Locate every Plasmodium parasite.
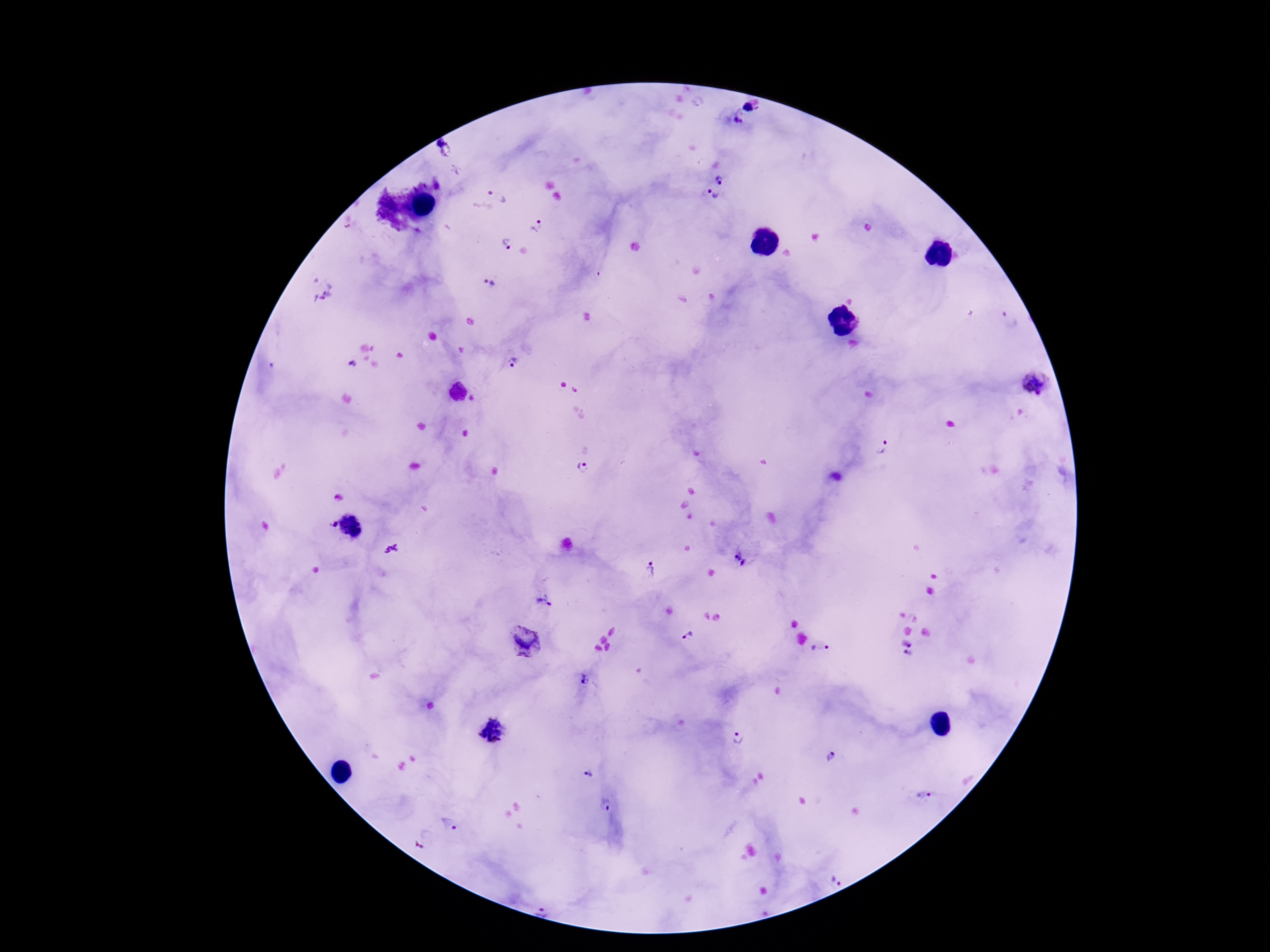
Approximate centers as {x, y} in pixels.
Plasmodium parasites: {748, 107}, {739, 123}, {444, 146}, {721, 181}, {499, 190}, {712, 196}, {537, 225}, {505, 244}, {490, 284}, {1009, 319}, {513, 363}, {352, 365}, {1037, 384}, {883, 448}, {583, 469}, {334, 525}, {351, 526}, {741, 560}, {651, 570}, {544, 599}, {689, 637}, {907, 643}, {525, 644}, {821, 649}, {909, 654}, {582, 680}, {494, 730}, {738, 738}, {832, 756}, {588, 777}, {926, 794}, {607, 804}, {449, 824}, {423, 839}, {835, 881}, {545, 904}.

patient malaria status = positive
image size = 1270×952 pixels
preparation = thick blood film
capture = smartphone camera through the microscope eyepiece
stain = Giemsa
magnification = 100x
field of view = one from this slide